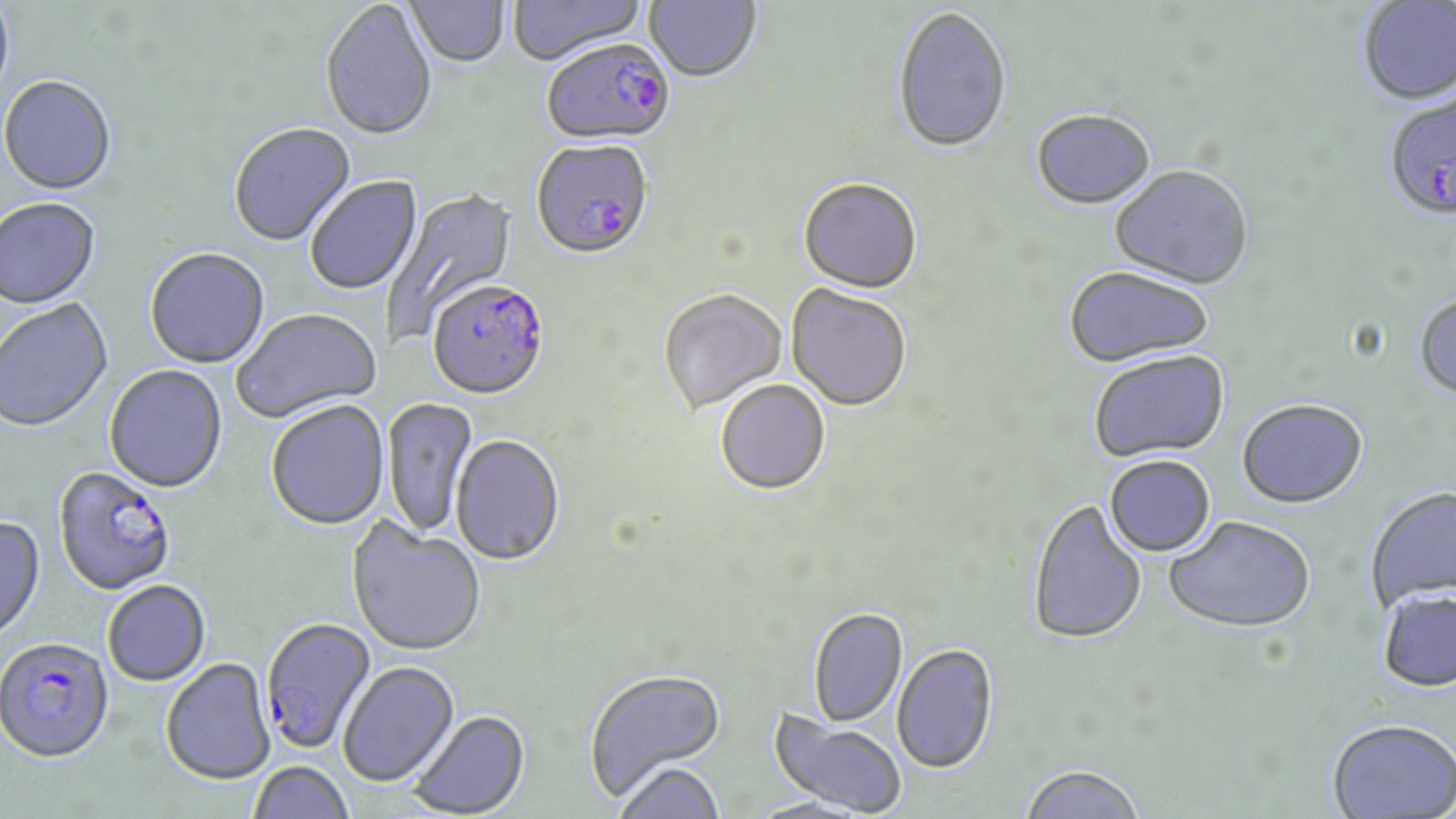

slide_level_diagnosis: Plasmodium falciparum
preparation: thin blood film
image_size: 1456×819 pixels
modality: light microscopy
stain: May-Grünwald-Giemsa
field_of_view: one of a larger specimen
magnification: 1000x
uninfected_red_blood_cell_locations: 'approximate bounding boxes as (x1,y1)-(x2,y2) corner pairs in pixels: (0,0)-(15,110), (507,0)-(646,68), (644,0)-(761,85), (320,1)-(437,143), (405,1)-(510,70), (1358,1)-(1456,107), (893,9)-(1012,156), (0,78)-(117,197), (1031,112)-(1156,212), (229,124)-(356,248), (1110,167)-(1254,292), (305,176)-(423,296), (798,180)-(923,296), (381,185)-(518,342), (0,199)-(101,311), (145,250)-(270,370), (1064,268)-(1213,369), (785,285)-(911,414), (658,290)-(788,416), (1415,293)-(1456,402), (0,298)-(114,435), (231,310)-(383,426), (1089,352)-(1230,464), (104,365)-(228,495), (716,381)-(831,497), (382,397)-(478,539), (266,401)-(390,532), (1237,401)-(1369,511), (451,435)-(565,568), (1105,456)-(1216,558), (1365,487)-(1456,613), (1028,500)-(1147,647), (0,516)-(46,645), (1164,517)-(1315,636), (346,519)-(486,658), (103,581)-(210,687), (1376,590)-(1456,695), (809,609)-(908,728), (892,644)-(998,775), (161,659)-(276,787), (338,662)-(460,788), (583,667)-(727,801), (767,709)-(907,817), (409,711)-(531,818), (1326,720)-(1456,819), (249,761)-(354,818), (615,761)-(725,819), (1018,765)-(1146,819)'
plasmodium_falciparum_infected_red_blood_cell_locations: 'approximate bounding boxes as (x1,y1)-(x2,y2) corner pairs in pixels: (542,40)-(676,148), (1382,92)-(1456,225), (531,141)-(654,263), (428,282)-(549,402), (53,466)-(178,597), (260,617)-(377,754), (0,638)-(115,764)'